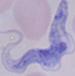
magnification = 1000x
modality = micrograph
identification = trypanosome